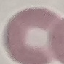

Summary:
  - Malaria status: uninfected
  - Capture: smartphone camera at the microscope eyepiece
  - Stain: Giemsa
  - Image type: automatically extracted cell patch, resized to 64 × 64 pixels
  - Preparation: thin blood smear